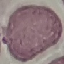

Malaria status: uninfected. Thin blood smear. Automatically extracted cell patch, resized to 64 × 64 pixels. Acquired by smartphone through the microscope eyepiece. Giemsa stain.